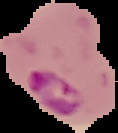
Summary:
  - Result: malaria parasites detected
  - Image size: 118×133 pixels
  - Preparation: thin blood film
  - Image type: segmented cell region on a black background